Give the position of every Plasmodium falciparum parasite, noting its life-cycle stage.
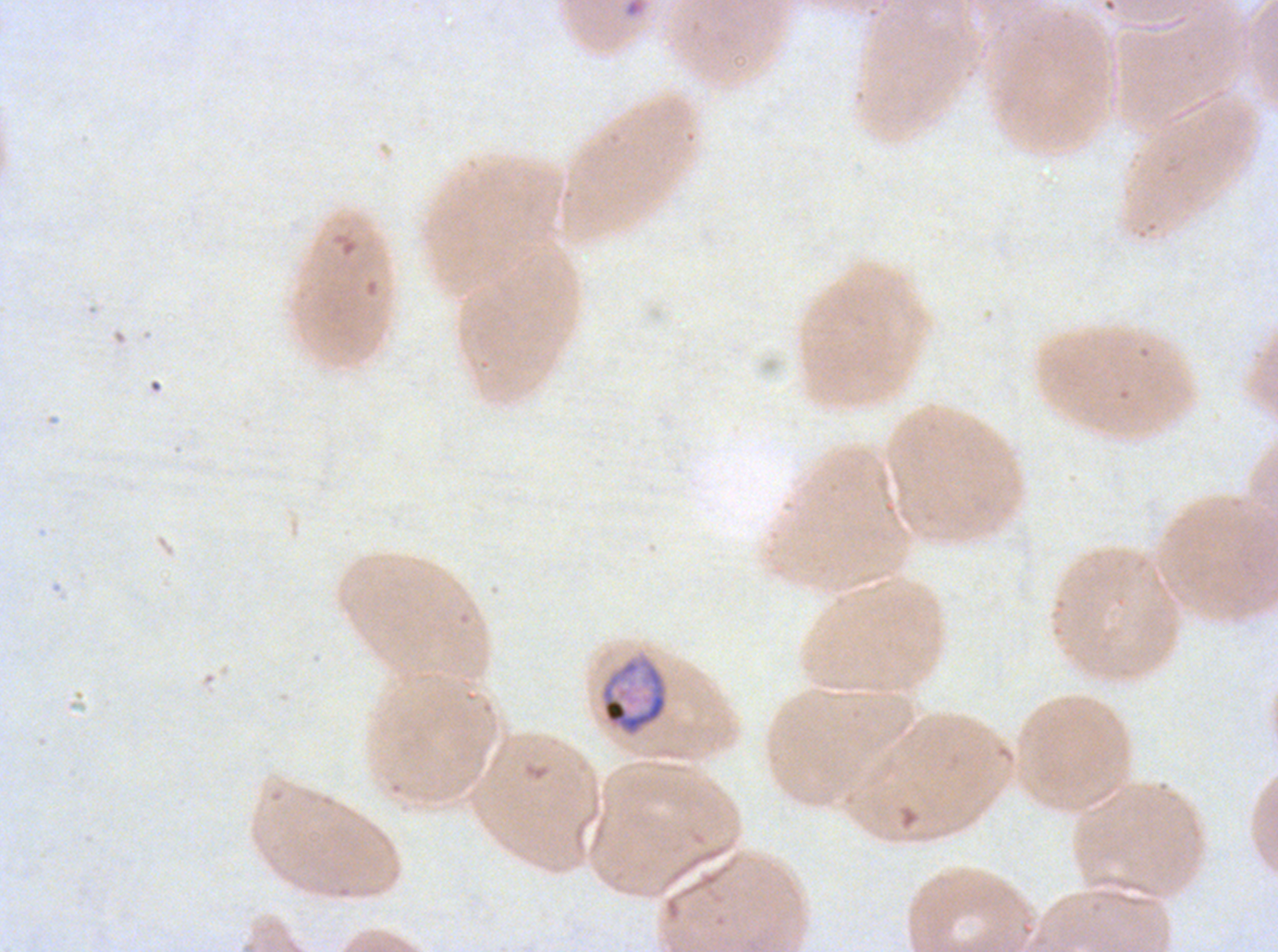
Approximate bounding rectangles given as corner coordinates in pixels from the top-left.
Late trophozoites: (x1=599, y1=657, x2=669, y2=737).
No rings, late-ring/early-trophozoite forms, mid trophozoites, early schizonts, late schizonts, segmenters, or gametocytes observed.

Image is 1278×952 pixels. Giemsa-stained preparation. Thin blood film. Plasmodium falciparum from a patient in The Gambia, cultured ex vivo for 24 to 48 hours. A sub-image separated from a larger composite.